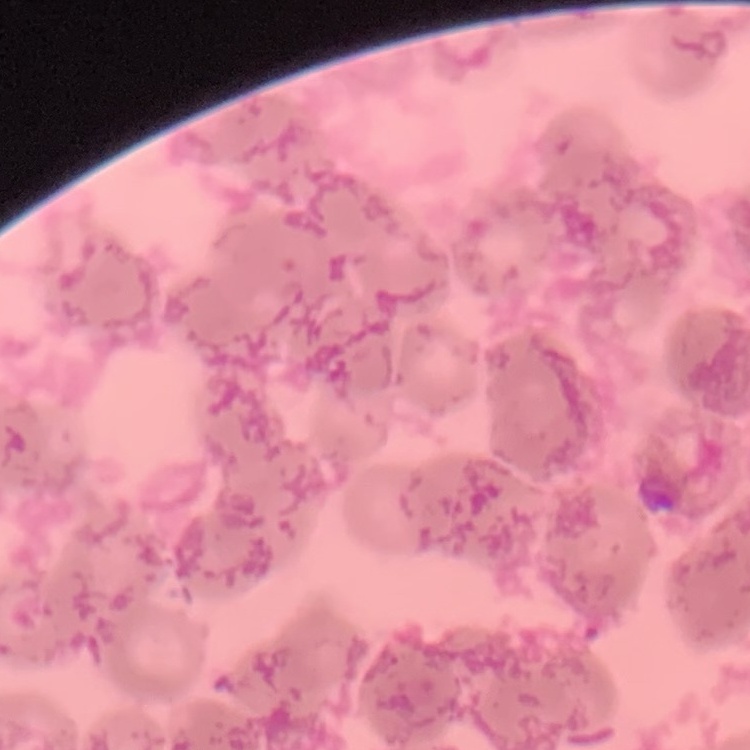 The red blood cells show rouleaux formation. Field's or Giemsa stain. One tile cut from a larger photomicrograph. Thin blood smear.